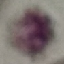
Summary:
  - Result: negative for malaria parasites
  - Stain: Giemsa
  - Preparation: thin smear
  - Image type: cell patch, automatically extracted from a larger field of view and resized to 64 × 64 pixels
  - Capture: smartphone camera at the microscope eyepiece